Comment on the morphology of the erythrocytes.
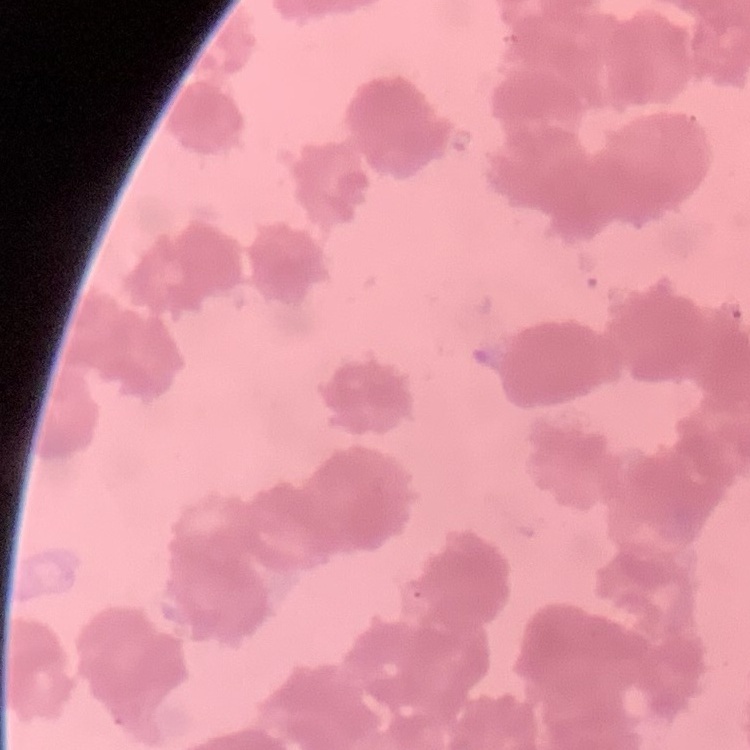

Rouleaux formation.

Field's or Giemsa stain. One tile cut from a larger photomicrograph. Thin blood film.